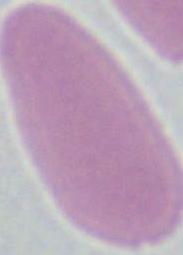
Summary:
  - Magnification: 1000x
  - Identification: erythrocyte
  - Modality: photomicrograph